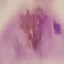

Malaria status: parasitized. Photographed with a smartphone camera at the microscope eyepiece. Giemsa stain. Thin blood smear. Cell patch, automatically extracted from a larger field of view and resized to 64 × 64 pixels.